State which cell type is depicted.
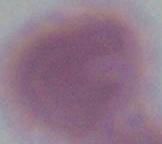
An erythrocyte.

Micrograph. 1000x magnification.